Report the malaria status of this cell.
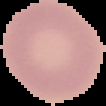

It is uninfected.

Summary:
  - Image type: cell region segmented out of the field of view; surrounding area masked to black
  - Image size: 106×106 pixels
  - Preparation: thin blood film